Describe the morphology of the red blood cells.
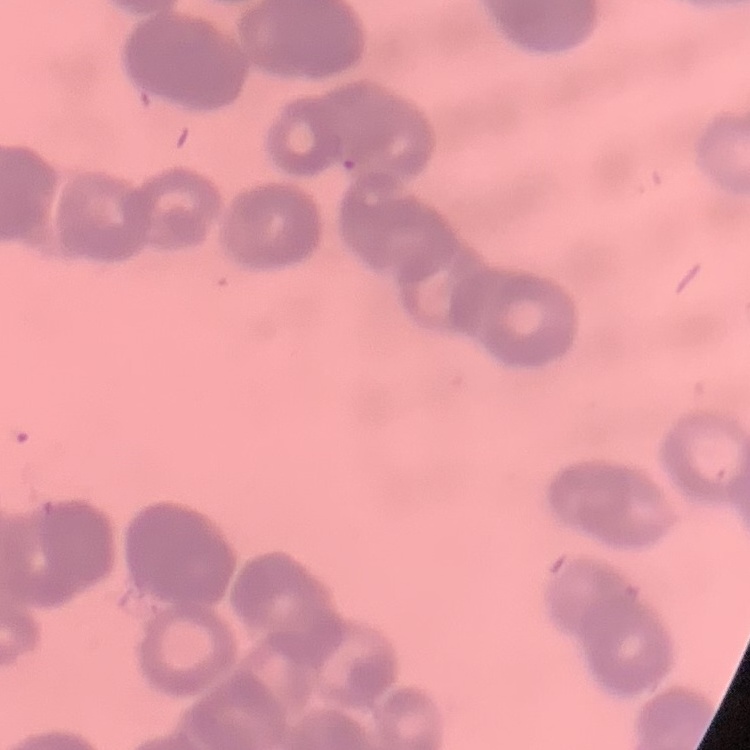

They show rouleaux formation.

stain = Field's or Giemsa
image type = one tile cut from a larger photomicrograph
preparation = thin blood film